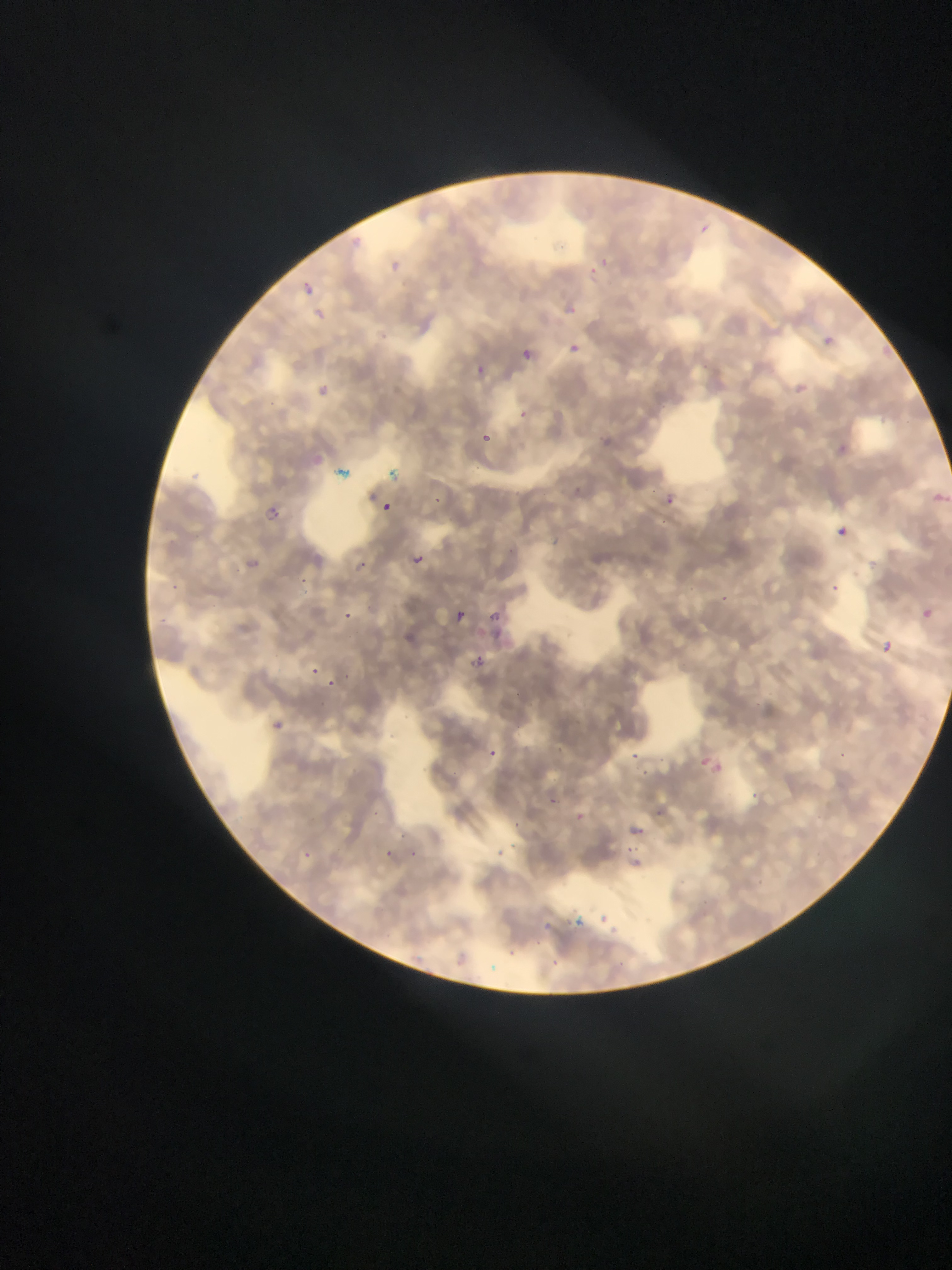
Approximate bounding boxes as {left, top, right, bottom} in pixels.
Summary:
  - Malaria parasite locations: {697, 219, 716, 235}, {350, 230, 380, 250}, {391, 249, 409, 270}, {600, 251, 614, 269}, {580, 258, 610, 280}, {298, 282, 331, 306}, {563, 295, 590, 325}, {311, 302, 333, 324}, {816, 333, 847, 355}, {514, 340, 539, 362}, {567, 342, 582, 356}, {473, 359, 489, 381}, {799, 375, 815, 397}, {313, 384, 338, 400}, {521, 406, 539, 424}, {872, 408, 882, 420}, {475, 430, 493, 452}, {823, 442, 864, 463}, {373, 460, 410, 490}, {326, 466, 352, 481}, {926, 488, 948, 510}, {657, 491, 680, 512}, {429, 493, 446, 513}, {381, 501, 393, 513}, {263, 502, 294, 524}, {836, 527, 848, 538}, {407, 551, 432, 575}, {347, 554, 371, 576}, {298, 575, 315, 593}, {828, 575, 848, 593}, {716, 589, 748, 611}, {339, 602, 370, 620}, {446, 604, 469, 626}, {922, 605, 939, 619}, {484, 609, 508, 631}, {876, 639, 895, 657}, {466, 650, 491, 673}, {306, 663, 321, 675}, {337, 667, 361, 684}, {323, 678, 340, 690}, {264, 716, 286, 736}, {486, 741, 500, 760}, {633, 745, 644, 761}, {830, 748, 848, 764}, {695, 752, 728, 781}, {634, 767, 656, 784}, {755, 788, 766, 802}, {550, 791, 563, 805}, {578, 807, 585, 822}, {515, 816, 527, 830}, {630, 821, 667, 843}, {401, 825, 413, 843}, {507, 836, 526, 851}, {495, 842, 509, 860}, {385, 845, 403, 862}, {402, 845, 420, 860}, {625, 845, 650, 859}, {302, 846, 316, 862}, {595, 907, 620, 928}, {573, 911, 591, 930}, {540, 919, 565, 932}, {507, 941, 525, 957}, {450, 949, 474, 972}, {544, 952, 566, 973}
  - Field of view: single
  - Country: Ghana
  - Image size: 952×1270 pixels
  - Preparation: thin blood smear
  - Capture: mobile-phone photograph through a microscope